Classify this cell by malaria status.
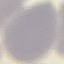

Uninfected.

Giemsa-stained preparation. Automatically extracted cell patch, resized to 64 × 64 pixels. Acquired by smartphone through the microscope eyepiece. Thin blood smear.